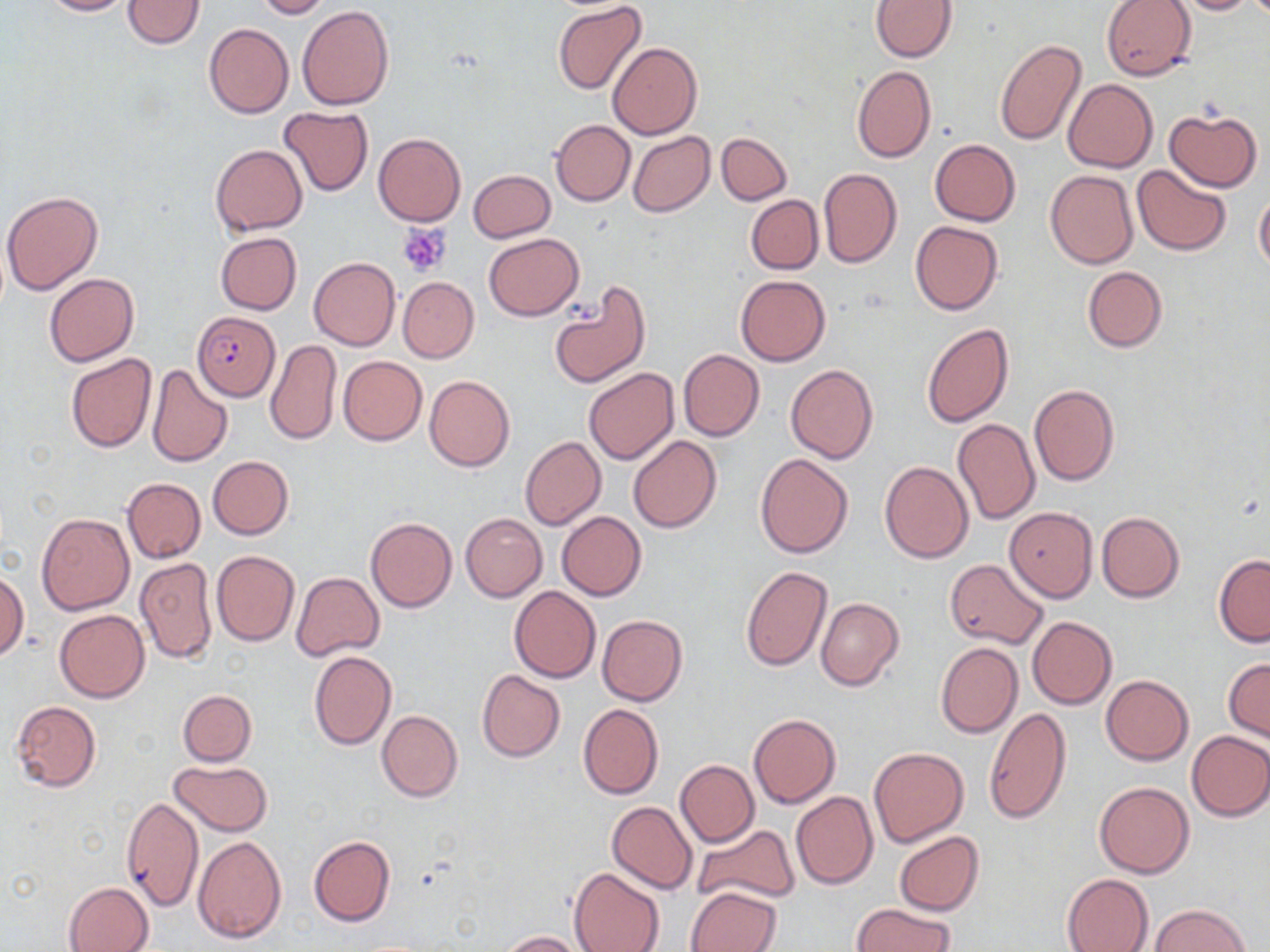

Approximate bounding boxes as (x1, y1, x2, y2) in pixels. Uninfected red blood cell locations: (38, 0, 135, 17), (122, 0, 204, 48), (254, 0, 330, 19), (1101, 0, 1198, 81), (1167, 0, 1259, 15), (870, 1, 956, 61), (552, 2, 647, 96), (297, 5, 393, 111), (203, 22, 295, 119), (994, 37, 1087, 147), (609, 42, 702, 139), (852, 66, 935, 162), (1062, 78, 1157, 172), (278, 106, 373, 195), (1164, 108, 1262, 192), (223, 119, 368, 220), (550, 120, 635, 205), (628, 131, 715, 217), (373, 133, 465, 226), (716, 133, 791, 206), (929, 139, 1020, 226), (210, 145, 307, 234), (1133, 165, 1232, 257), (818, 168, 902, 268), (468, 169, 555, 243), (1045, 170, 1137, 268), (1, 191, 104, 295), (1254, 191, 1270, 273), (746, 195, 823, 274), (910, 220, 1002, 314), (216, 232, 301, 315), (483, 233, 584, 320), (309, 257, 399, 350), (1082, 266, 1166, 353), (44, 273, 139, 367), (736, 275, 830, 367), (398, 277, 479, 362), (549, 283, 651, 389), (922, 324, 1014, 428), (265, 339, 341, 446), (678, 349, 764, 441), (65, 353, 156, 453), (339, 356, 426, 445), (146, 364, 233, 468), (786, 365, 877, 465), (583, 369, 679, 465), (424, 375, 515, 472), (1029, 384, 1119, 486), (952, 417, 1041, 526), (628, 435, 721, 533), (520, 436, 606, 529), (754, 452, 853, 557), (208, 456, 294, 539), (880, 461, 973, 564), (121, 477, 205, 563), (1004, 508, 1097, 602), (557, 511, 646, 599), (36, 512, 134, 615), (1097, 512, 1184, 602), (461, 513, 546, 602), (366, 518, 457, 613), (212, 551, 300, 646), (1213, 556, 1270, 647), (135, 558, 218, 664), (944, 558, 1048, 648), (740, 565, 833, 670), (0, 567, 27, 661), (292, 572, 384, 660), (509, 586, 601, 682), (816, 597, 904, 691), (55, 610, 149, 702), (597, 615, 687, 707), (1027, 616, 1116, 709), (936, 642, 1023, 738), (309, 651, 396, 749), (1223, 658, 1270, 742), (477, 669, 566, 762), (1101, 675, 1194, 765), (178, 690, 257, 765), (11, 700, 102, 791), (578, 703, 664, 799), (985, 707, 1072, 824), (376, 710, 463, 802), (748, 714, 841, 807), (1185, 730, 1270, 822), (868, 746, 969, 848), (168, 760, 274, 835), (675, 760, 759, 847), (1095, 781, 1194, 878), (791, 791, 877, 889), (121, 795, 204, 912), (607, 801, 698, 893), (134, 812, 252, 930), (692, 823, 799, 908), (894, 831, 984, 916), (193, 834, 286, 942), (309, 836, 396, 927), (568, 868, 664, 952), (1061, 873, 1154, 952), (63, 881, 152, 952), (688, 886, 782, 952), (851, 903, 954, 952), (1150, 904, 1251, 951), (498, 930, 587, 951). Plasmodium falciparum-infected red blood cell locations: (193, 311, 280, 402). Platelet locations: (398, 222, 452, 277). Slide-level diagnosis: Plasmodium falciparum. Light microscopy. May-Grünwald-Giemsa-stained preparation. Image is 1270×952 pixels. Thin blood film. 1000x magnification. One field of a larger specimen.